Assess this cell for malaria.
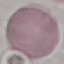

Uninfected.

Summary:
  - Preparation: thin blood smear
  - Image type: cell patch, automatically extracted from a larger field of view and resized to 64 × 64 pixels
  - Capture: smartphone through the microscope eyepiece
  - Stain: Giemsa